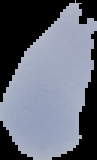
image type = segmented cell region with the area outside set to black
image size = 97×160 pixels
malaria status = uninfected
preparation = thin blood smear